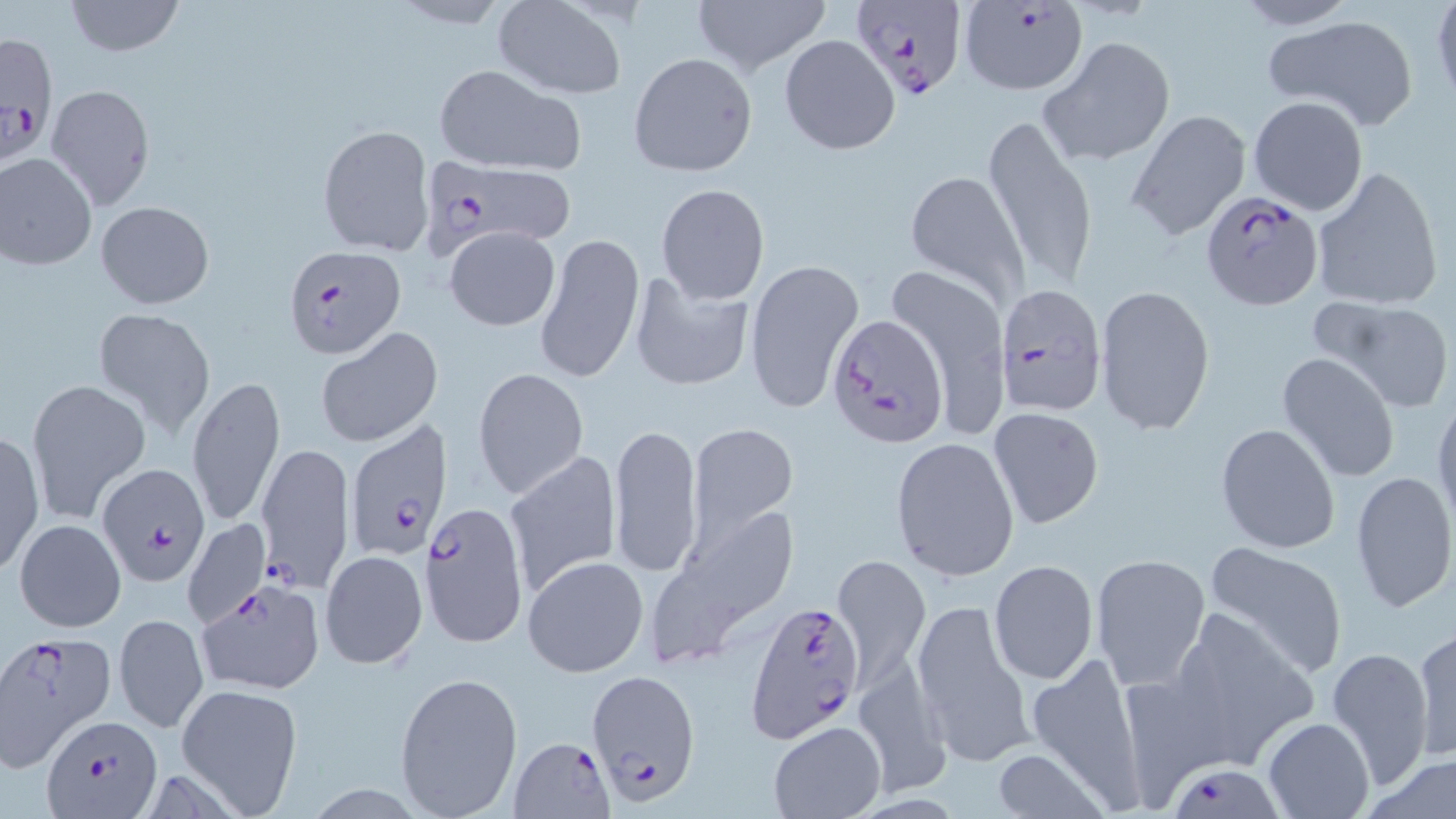

Summary:
  - Coordinate format: approximate bounding boxes as (x1, y1, x2, y2) in pixels
  - Uninfected red blood cell locations: (62, 0, 188, 56), (690, 0, 832, 78), (1429, 0, 1456, 109), (1229, 1, 1362, 30), (494, 2, 624, 97), (1263, 16, 1419, 129), (779, 34, 899, 156), (1038, 36, 1175, 169), (630, 53, 757, 177), (431, 64, 584, 175), (45, 84, 155, 210), (1249, 95, 1370, 215), (982, 115, 1098, 292), (317, 124, 435, 257), (0, 152, 99, 270), (1310, 165, 1444, 311), (905, 169, 1029, 303), (656, 183, 770, 305), (95, 200, 215, 309), (445, 225, 560, 331), (534, 231, 645, 385), (741, 257, 864, 413), (884, 263, 1012, 436), (626, 274, 754, 395), (1094, 285, 1215, 435), (1321, 298, 1454, 412), (92, 306, 215, 440), (316, 327, 442, 448), (1276, 352, 1401, 483), (472, 367, 588, 500), (185, 376, 285, 527), (26, 378, 151, 522), (1431, 393, 1456, 533), (988, 406, 1104, 530), (609, 421, 703, 579), (689, 422, 797, 535), (1215, 423, 1341, 554), (1, 430, 45, 576), (891, 436, 1020, 582), (505, 451, 622, 595), (1350, 470, 1455, 614), (654, 499, 803, 658), (182, 518, 269, 628), (14, 519, 126, 632), (1201, 539, 1351, 678), (319, 549, 428, 671), (1089, 554, 1210, 690), (522, 555, 650, 678), (832, 555, 930, 691), (988, 559, 1099, 684), (911, 600, 1034, 765), (1166, 605, 1321, 768), (114, 611, 208, 733), (1412, 627, 1455, 762), (1325, 650, 1434, 789), (1027, 652, 1148, 805), (853, 655, 950, 795), (394, 670, 524, 816), (175, 683, 304, 815), (1263, 717, 1374, 819), (769, 720, 886, 818), (988, 749, 1107, 819), (1359, 755, 1456, 817)
  - Plasmodium falciparum-infected red blood cell locations: (850, 0, 966, 101), (961, 0, 1088, 96), (1, 31, 59, 159), (1125, 108, 1251, 241), (427, 158, 574, 250), (1200, 191, 1324, 311), (283, 245, 405, 359), (994, 285, 1104, 417), (827, 313, 948, 448), (341, 417, 451, 562), (255, 440, 354, 593), (96, 461, 208, 586), (419, 500, 529, 649), (199, 581, 326, 694), (746, 602, 865, 740), (0, 633, 112, 765), (585, 672, 701, 806), (42, 711, 160, 818), (507, 740, 611, 819), (1176, 764, 1280, 819)
  - Slide-level diagnosis: Plasmodium falciparum
  - Magnification: 1000x
  - Preparation: thin blood smear
  - Modality: optical microscopy
  - Stain: May-Grünwald-Giemsa
  - Field of view: one of a larger specimen
  - Image size: 1456×819 pixels